Describe the morphology of the erythrocytes.
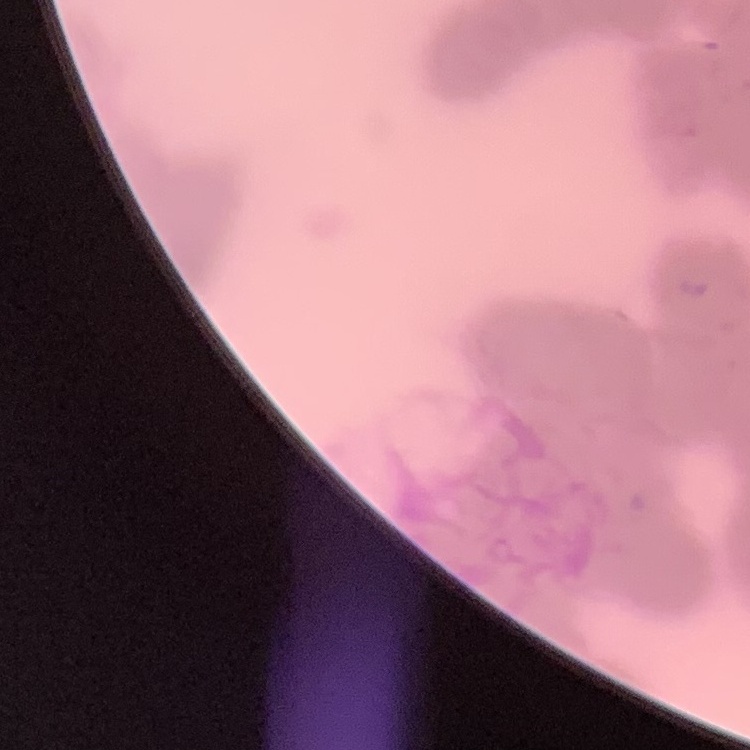
Rouleaux formation.

One tile cut from a larger photomicrograph. Stained with either Field's or Giemsa. Thin blood smear.